Assess this cell for malaria.
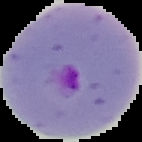

It is parasitized.

preparation = thin blood smear
image size = 142×142 pixels
image type = segmented cell region on a black background